Comment on the morphology of the red blood cells.
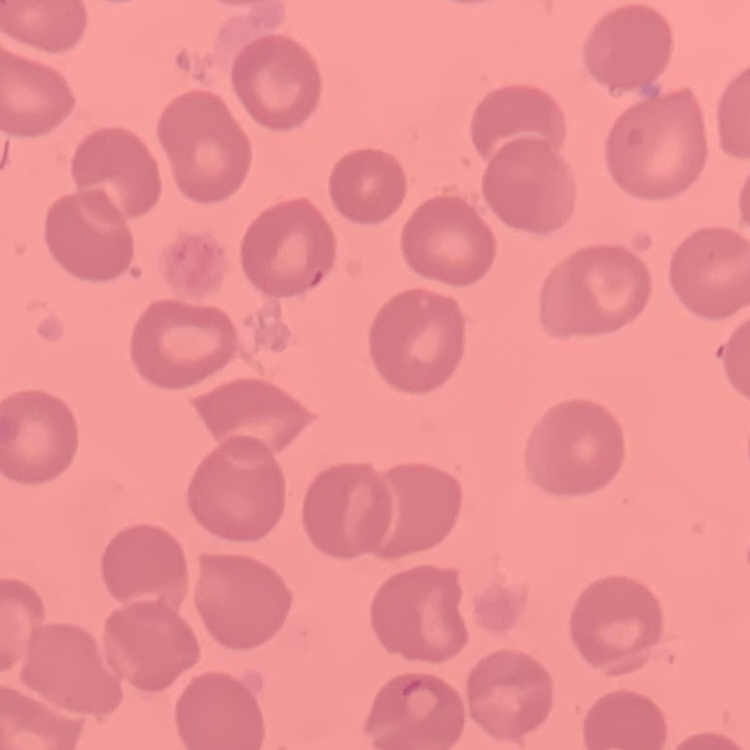
They show no rouleaux formation.

{
  "stain": "Field's or Giemsa",
  "image_type": "one tile cut from a larger photomicrograph",
  "preparation": "thin peripheral smear"
}